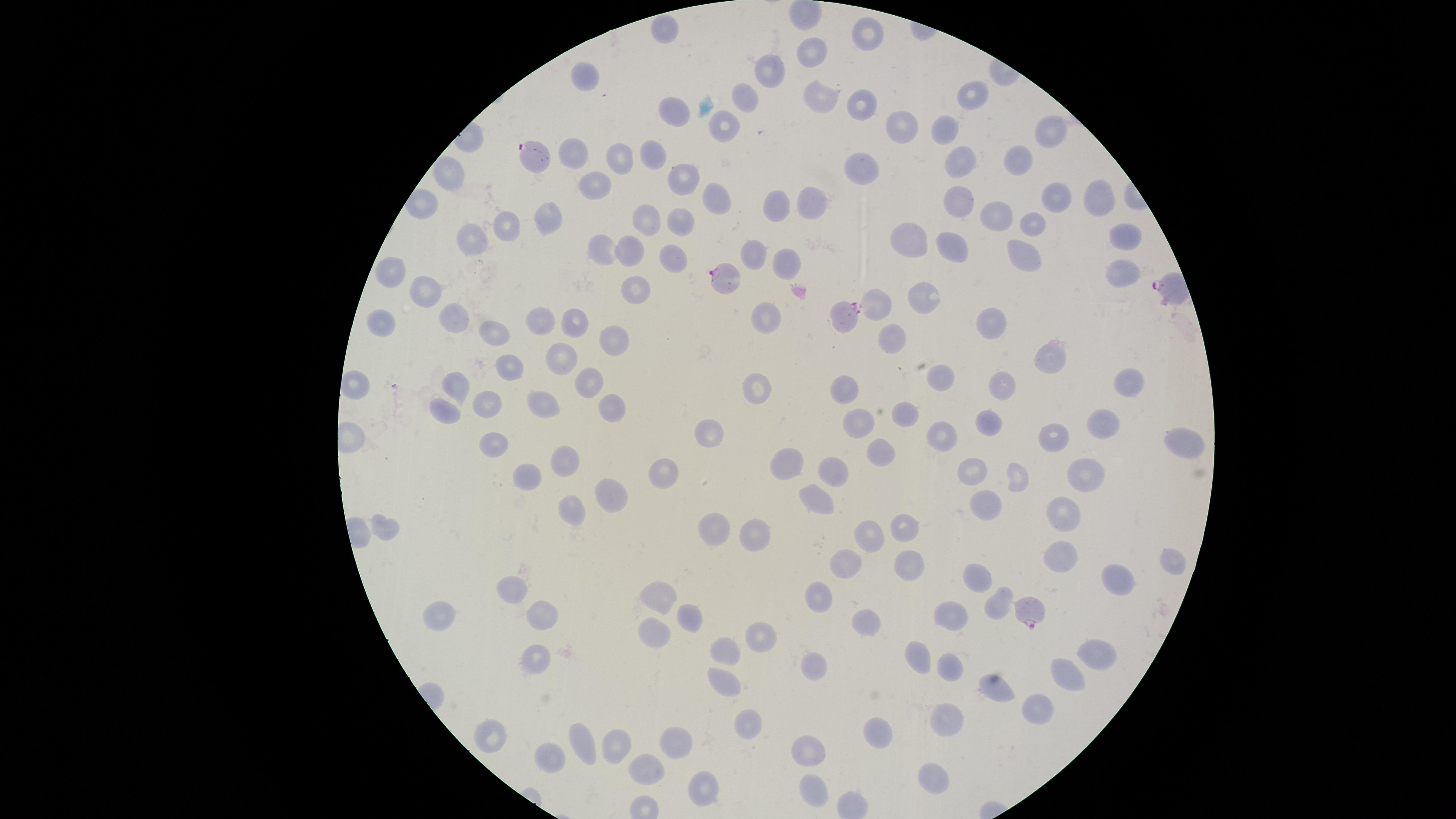

Approximate marker points as [x, y] in pixels.
Summary:
  - Uninfected red blood cells: [804, 12], [664, 30], [866, 33], [808, 49], [769, 71], [589, 77], [972, 92], [820, 95], [858, 105], [675, 107], [901, 125], [1048, 130], [946, 131], [575, 152], [617, 157], [960, 157], [1017, 159], [655, 160], [866, 166], [685, 176], [452, 177], [600, 183], [960, 197], [716, 198], [1098, 198], [1050, 201], [423, 203], [775, 203], [808, 204], [998, 212], [645, 214], [550, 218], [686, 219], [1032, 224], [506, 227], [908, 235], [1118, 236], [954, 237], [475, 243], [606, 247], [632, 247], [1030, 250], [757, 253], [672, 255], [782, 258], [1117, 269], [396, 271], [423, 289], [634, 289], [926, 297], [874, 299], [763, 316], [578, 317], [457, 319], [546, 320], [994, 322], [386, 324], [493, 330], [892, 334], [619, 336], [565, 353], [1047, 361], [509, 375], [840, 383], [942, 383], [454, 384], [594, 384], [758, 386], [1125, 386], [364, 387], [1001, 387], [492, 400], [548, 403], [607, 405], [450, 406], [908, 413], [860, 418], [990, 421], [941, 425], [1100, 427], [712, 428], [1055, 434], [1177, 440], [490, 442], [879, 451], [790, 459], [565, 463], [831, 467], [971, 468], [661, 472], [518, 473], [1085, 476], [1022, 479], [611, 494], [814, 494], [982, 501], [566, 512], [1061, 512], [718, 523], [903, 526], [387, 529], [752, 532], [868, 536], [1058, 552], [910, 559], [1170, 559], [845, 563], [1112, 580], [979, 581], [519, 588], [999, 595], [820, 596], [669, 597], [441, 613], [951, 613], [546, 615], [689, 620], [863, 624], [657, 628], [761, 631], [725, 649], [1094, 652], [925, 655], [538, 663], [949, 664], [1069, 670], [816, 671], [722, 675], [999, 685], [1037, 704], [950, 716], [747, 724], [495, 735], [887, 738], [675, 740], [584, 742], [621, 743], [808, 751], [552, 753], [651, 766], [937, 777], [703, 784], [815, 789]
  - Parasitized red blood cells: [536, 156], [723, 282], [851, 315], [1031, 610]
  - Species: Plasmodium falciparum
  - Visible region: circular
  - Capture: smartphone photograph through the microscope eyepiece
  - Stain: Giemsa
  - Image size: 1456×819 pixels
  - Field of view: single
  - Preparation: thin blood film
  - Presence: malaria parasites identified